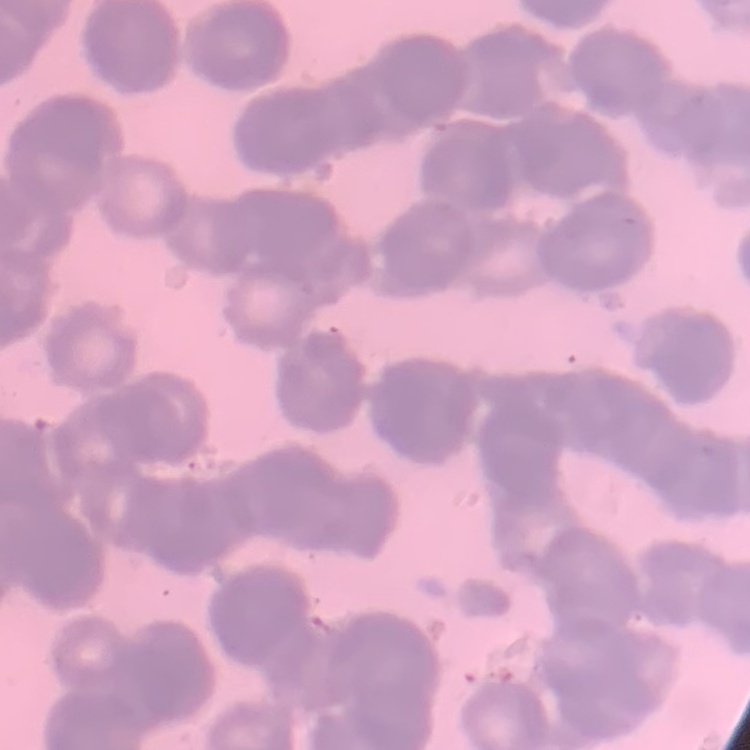
The erythrocytes exhibit rouleaux formation. Thin blood film. One tile cut from a larger photomicrograph. Stained with either Field's or Giemsa.